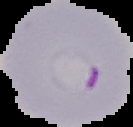

Summary:
  - Preparation: thin blood smear
  - Malaria status: parasitized
  - Image type: segmented cell region on a black background
  - Image size: 133×127 pixels